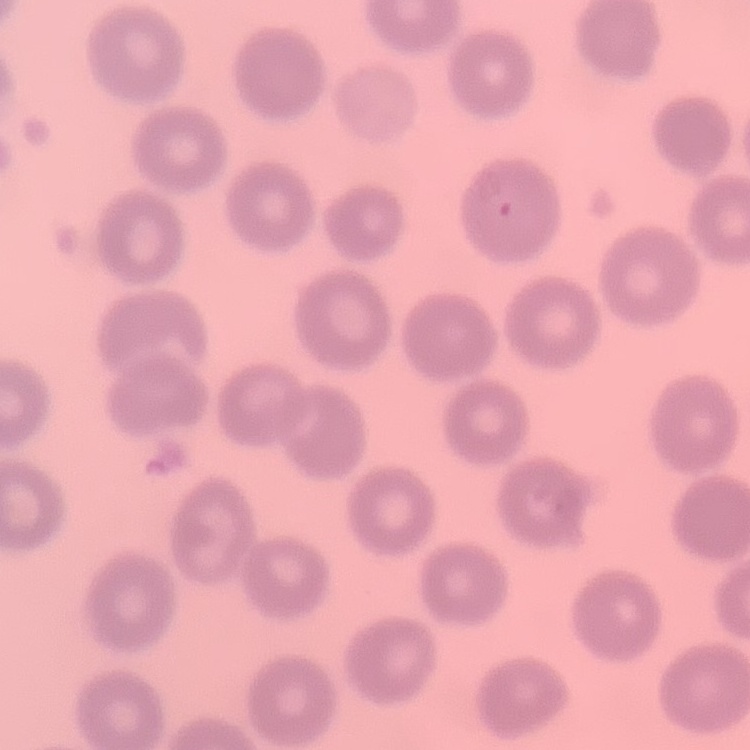

erythrocyte morphology = no rouleaux formation
preparation = thin blood smear
stain = Field's or Giemsa
image type = square crop of a larger photomicrograph